Report the malaria status of this cell.
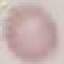
It is uninfected.

{
  "preparation": "thin blood film",
  "stain": "Giemsa",
  "capture": "smartphone through the microscope eyepiece",
  "image_type": "cell patch, automatically extracted from a larger field of view and resized to 64 × 64 pixels"
}